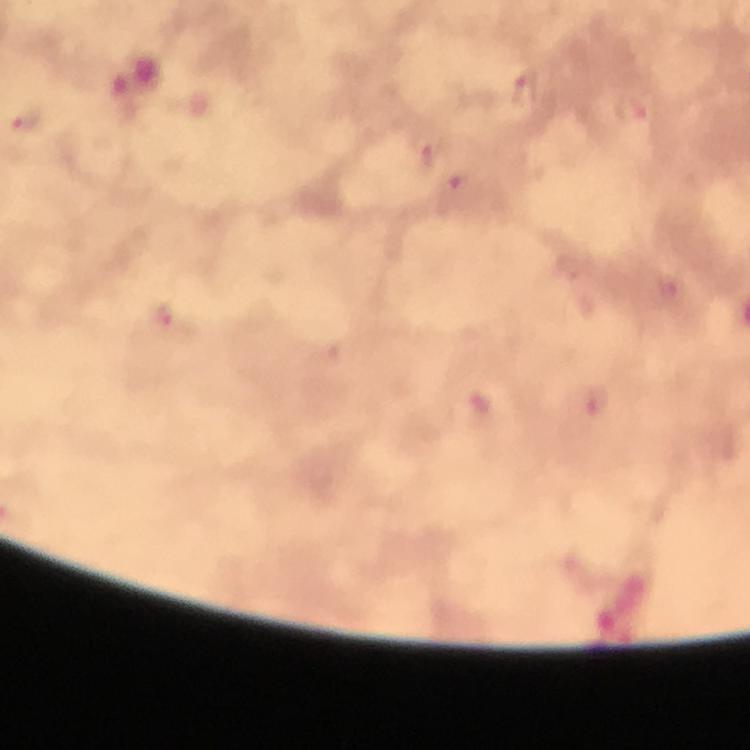 Approximate centers as {x, y} in pixels. Plasmodium parasite locations: {526, 90}, {633, 110}, {27, 121}, {428, 150}, {461, 182}, {163, 318}, {593, 404}. Giemsa-stained preparation. A crop from one field of view. From a malaria diagnostic workup. At 100x magnification. Photographed through the microscope with a smartphone camera. Immersion oil applied. Thick blood smear. Image is 750×750 pixels.